State the blood parasite species.
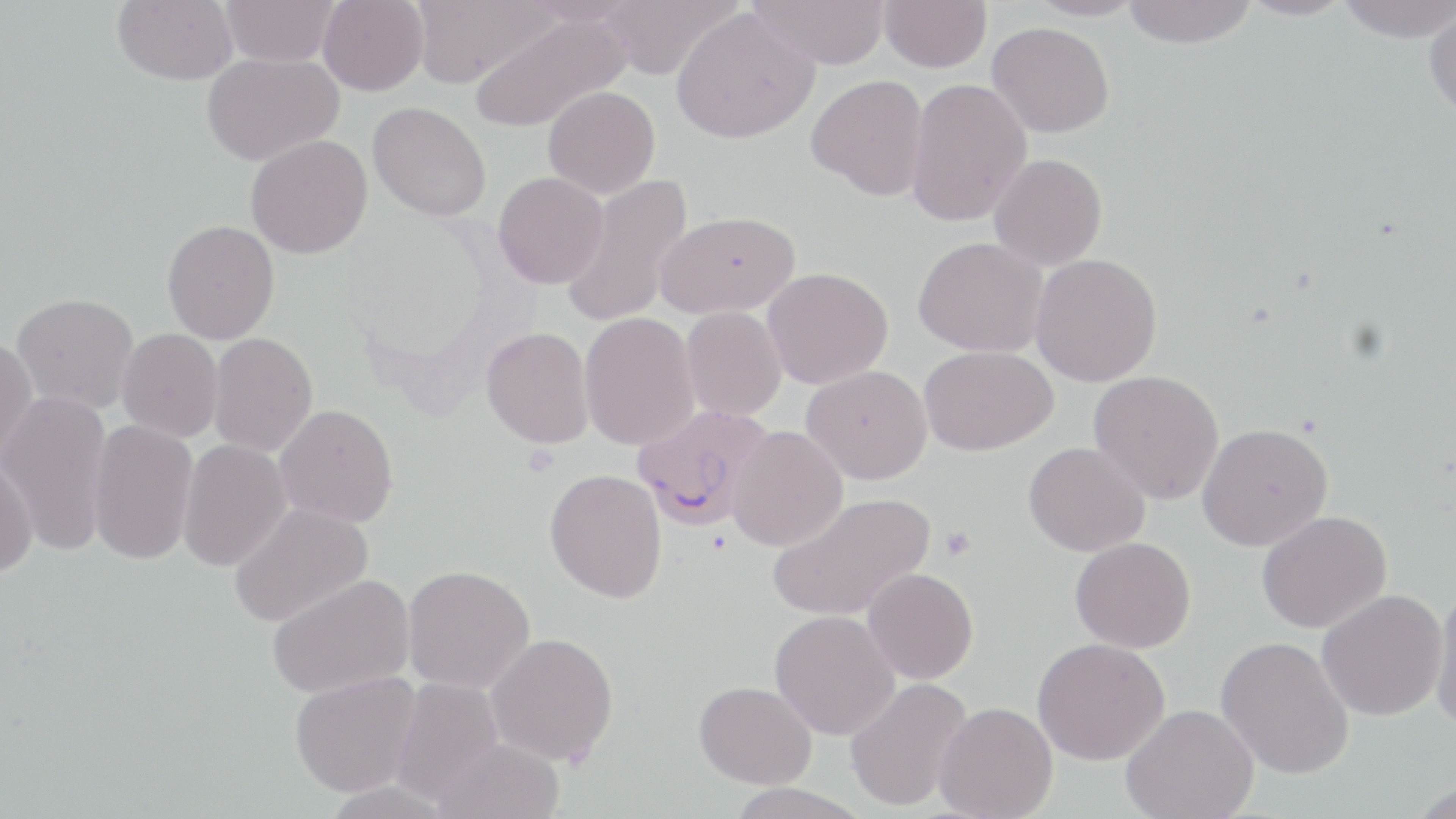
Plasmodium falciparum.

Approximate bounding boxes as (x1,y1)-(x2,y2) corner pairs in pixels. Platelet locations: (940,526)-(975,560). Plasmodium falciparum-infected red blood cell locations: (631,403)-(776,531). Uninfected red blood cell locations: (112,0)-(238,85), (220,0)-(339,66), (319,0)-(428,95), (410,0)-(558,87), (525,0)-(641,26), (598,0)-(741,79), (747,0)-(891,70), (879,0)-(991,72), (1026,0)-(1148,22), (1121,0)-(1259,49), (1236,0)-(1356,21), (1337,0)-(1454,42), (671,7)-(819,144), (1425,7)-(1456,123), (470,11)-(632,133), (987,22)-(1114,138), (202,53)-(343,165), (806,75)-(929,201), (905,78)-(1032,227), (542,86)-(660,198), (367,101)-(491,221), (245,134)-(372,259), (989,153)-(1108,270), (493,172)-(609,289), (560,174)-(695,329), (655,211)-(799,319), (162,219)-(280,344), (914,236)-(1047,357), (1030,253)-(1162,387), (762,267)-(894,389), (10,292)-(139,414), (680,306)-(787,421), (579,312)-(700,450), (481,327)-(595,449), (116,328)-(223,442), (208,332)-(318,457), (0,336)-(38,467), (918,345)-(1057,456), (802,365)-(933,484), (1088,370)-(1224,505), (1,391)-(112,557), (275,404)-(399,528), (87,419)-(198,566), (1197,423)-(1334,551), (727,425)-(847,551), (177,439)-(293,572), (1023,441)-(1149,557), (0,458)-(38,579), (545,468)-(667,603), (766,492)-(936,623), (228,502)-(372,627), (1256,510)-(1392,633), (1070,537)-(1197,653), (402,565)-(535,693), (863,567)-(978,684), (267,574)-(414,699), (1430,584)-(1456,734), (1316,589)-(1448,722), (769,610)-(900,740), (486,632)-(619,766), (1214,635)-(1355,780), (1032,637)-(1170,765), (288,671)-(421,797), (389,677)-(505,806), (845,677)-(973,812), (694,681)-(817,789), (933,702)-(1058,819), (1120,704)-(1259,819), (433,736)-(565,819), (1408,779)-(1455,819), (723,783)-(871,819). May-Grünwald-Giemsa-stained preparation. Thin blood film. Image is 1456×819 pixels. Single field of view. 1000x magnification. Light microscopy.